State which cell type is depicted.
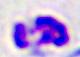
A leukocyte.

modality = micrograph
magnification = 400x